Name the cell type shown.
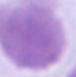
An erythrocyte.

Summary:
  - Magnification: 1000x
  - Modality: micrograph